Outline each blood parasite and name the species.
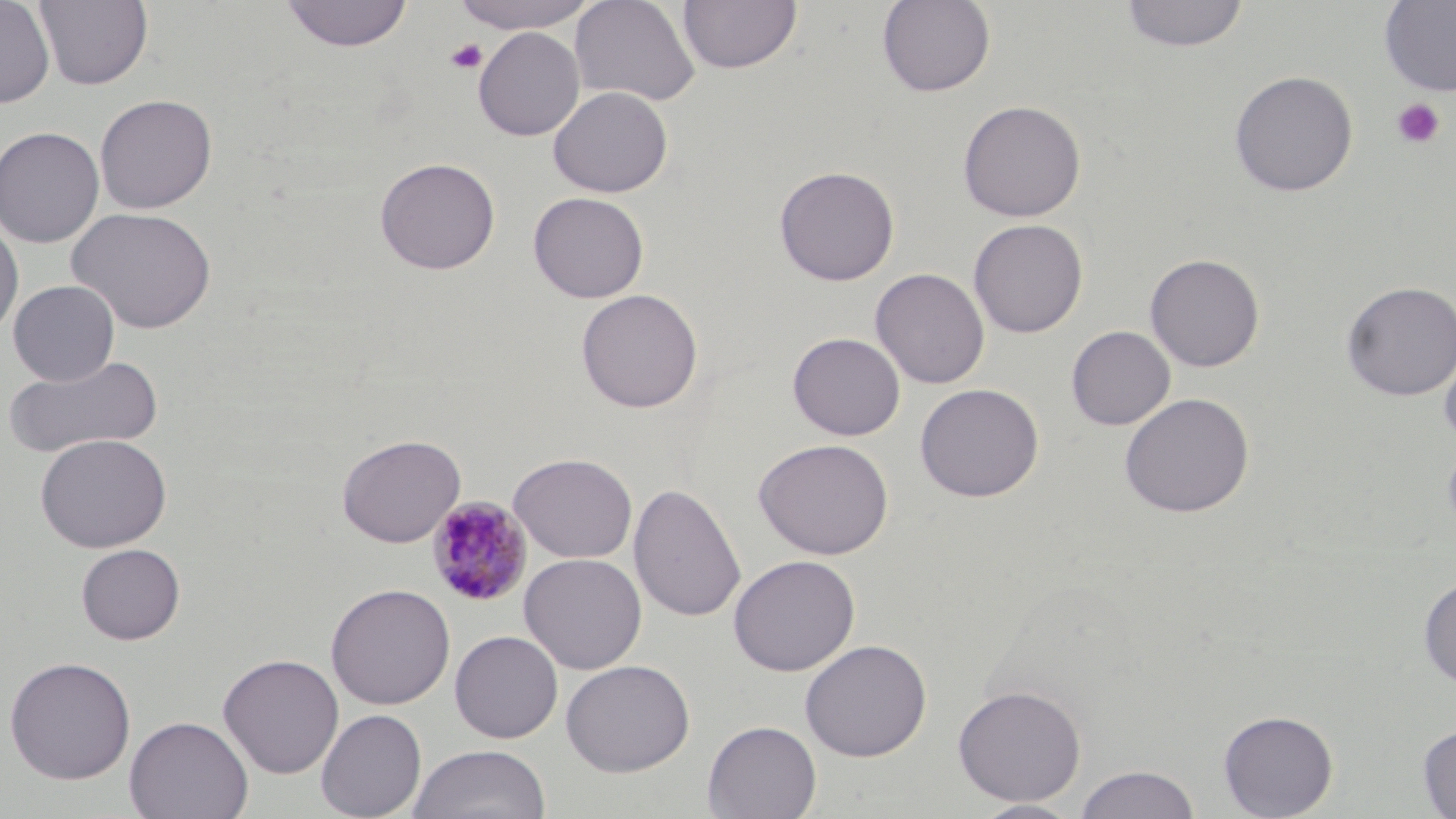

Approximate bounding boxes as [x1, y1, x2, y2] in pixels.
Plasmodium malariae-infected red blood cells: [427, 496, 533, 608].
No Plasmodium falciparum, Plasmodium ovale, Plasmodium vivax, Babesia divergens, or Trypanosoma brucei observed.

Summary:
  - Uninfected red blood cell locations: [0, 0, 55, 108], [35, 0, 154, 90], [278, 0, 413, 52], [449, 0, 603, 34], [569, 0, 701, 106], [677, 0, 802, 75], [876, 0, 997, 97], [1120, 0, 1249, 53], [1378, 1, 1456, 96], [473, 27, 586, 141], [1229, 70, 1358, 197], [547, 86, 674, 198], [94, 93, 217, 214], [957, 99, 1087, 222], [0, 125, 105, 248], [374, 156, 500, 275], [773, 165, 900, 286], [528, 192, 649, 303], [67, 206, 217, 334], [0, 217, 24, 342], [968, 218, 1088, 338], [1145, 253, 1265, 372], [870, 268, 990, 389], [8, 280, 120, 386], [1341, 280, 1456, 401], [575, 288, 703, 413], [1066, 326, 1176, 430], [787, 332, 906, 441], [1439, 344, 1456, 452], [5, 353, 166, 459], [914, 383, 1045, 502], [1119, 392, 1255, 518], [35, 433, 171, 552], [337, 434, 465, 547], [753, 438, 894, 560], [1441, 440, 1456, 539], [508, 452, 637, 563], [628, 484, 746, 623], [76, 543, 185, 645], [519, 552, 647, 674], [728, 554, 861, 676], [1418, 576, 1456, 689], [326, 583, 455, 710], [449, 630, 563, 743], [800, 639, 932, 762], [218, 653, 344, 779], [3, 656, 136, 784], [561, 659, 695, 777], [952, 684, 1087, 806], [315, 708, 427, 819], [1218, 709, 1338, 818], [124, 715, 253, 819], [703, 719, 822, 819], [1417, 724, 1456, 818], [406, 744, 551, 819], [1074, 765, 1201, 819], [969, 799, 1084, 819]
  - Platelet locations: [444, 38, 488, 75], [1391, 99, 1445, 149]
  - Slide-level diagnosis: Plasmodium malariae
  - Magnification: 1000x
  - Modality: optical microscopy
  - Image size: 1456×819 pixels
  - Stain: May-Grünwald-Giemsa
  - Preparation: thin blood film
  - Field of view: one of a larger specimen